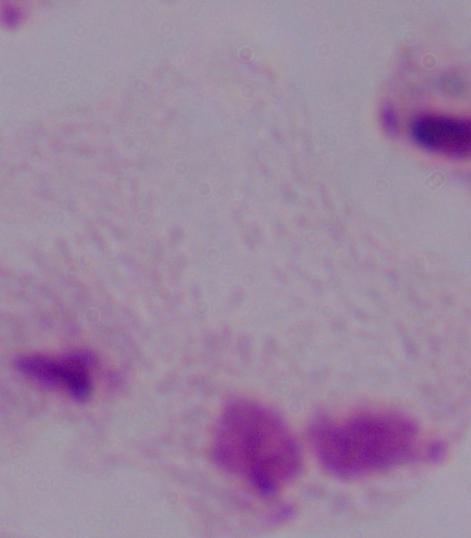

Summary:
  - Magnification: 1000x
  - Modality: micrograph
  - Identification: trichomonad